Assess this cell for malaria.
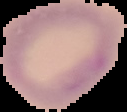

Uninfected.

image size = 127×112 pixels
image type = cell region segmented out of the field of view; surrounding area masked to black
preparation = thin blood smear